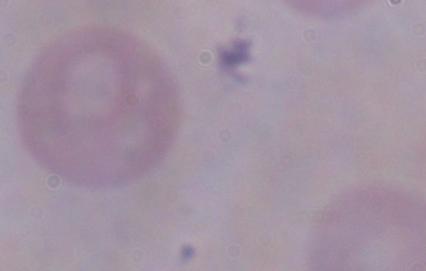 1000x magnification. A trypanosome is shown. Micrograph.